Report the malaria status of this cell.
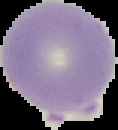

It is uninfected.

From a thin blood smear. Image is 118×130 pixels. The area outside the segmented cell region is set to black.